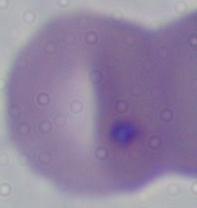

identification: Babesia
modality: micrograph
magnification: 1000x